Describe the morphology of the erythrocytes.
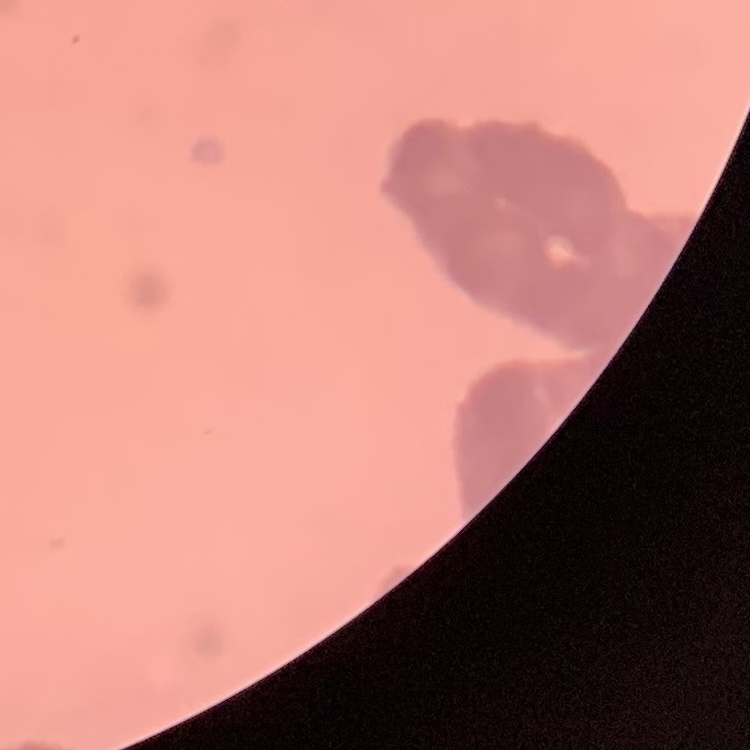
Rouleaux formation.

Summary:
  - Stain: Field's or Giemsa
  - Preparation: thin blood smear
  - Image type: one tile cut from a larger photomicrograph